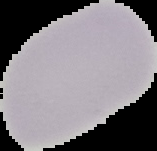 Image is 157×151 pixels. From a thin blood film. Cell region segmented out of the field of view; the surrounding area is masked to black. Result: negative for Plasmodium parasites.